State which parasite is depicted.
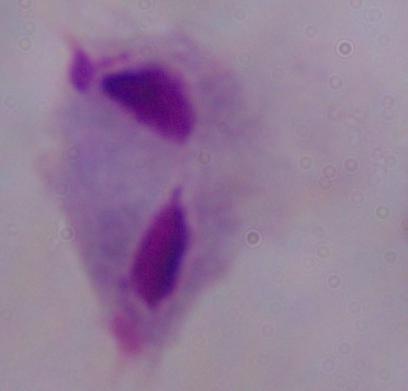
This is a trichomonad.

magnification: 1000x
modality: micrograph